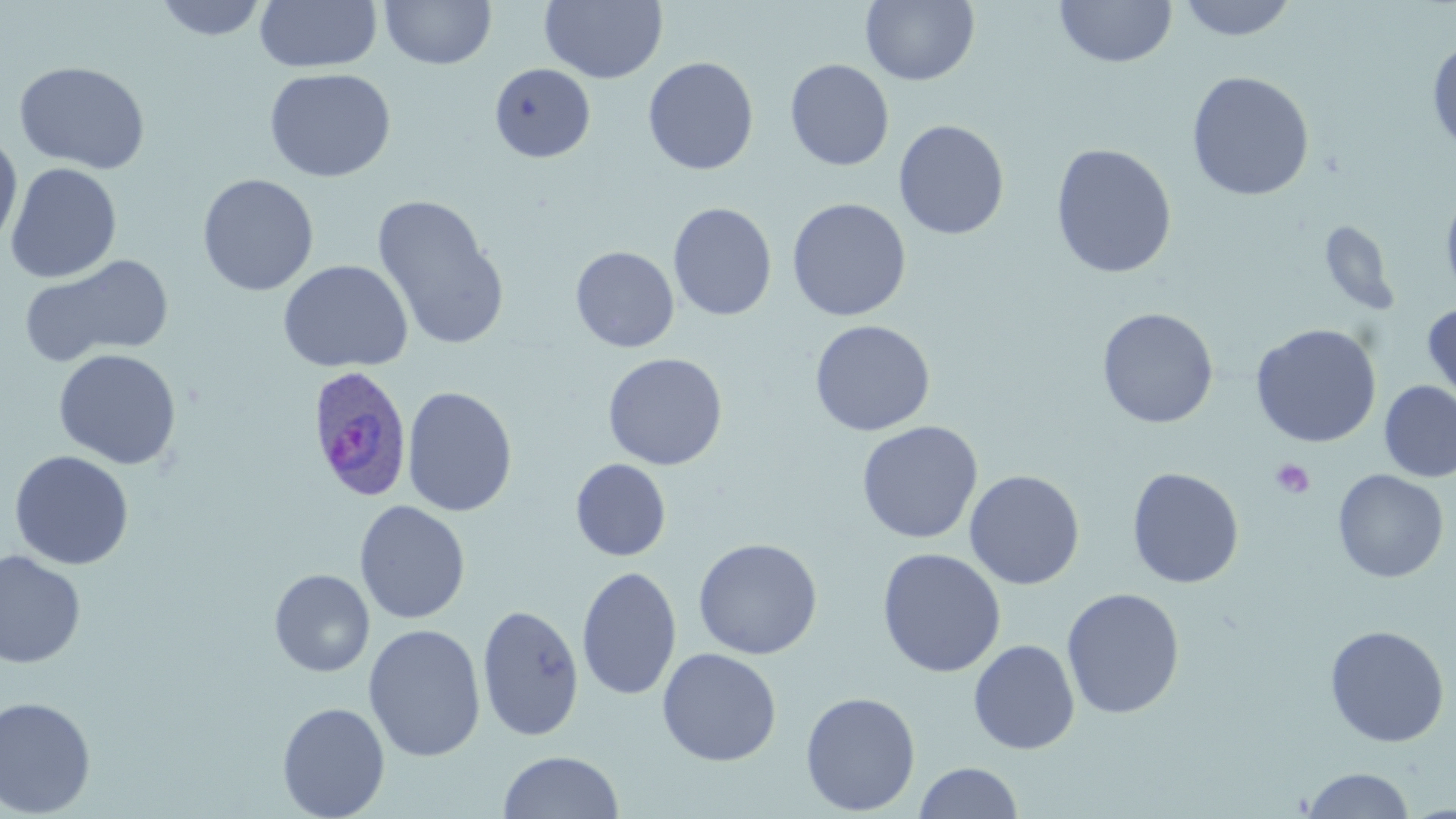

Summary:
  - Coordinate format: approximate bounding boxes as named x1/y1/x2/y2 corners in pixels
  - Uninfected red blood cell locations: (x1=154, y1=0, x2=269, y2=41), (x1=253, y1=0, x2=382, y2=73), (x1=380, y1=0, x2=497, y2=69), (x1=540, y1=0, x2=667, y2=84), (x1=1177, y1=0, x2=1298, y2=41), (x1=861, y1=1, x2=980, y2=86), (x1=1055, y1=1, x2=1177, y2=68), (x1=1427, y1=38, x2=1456, y2=156), (x1=643, y1=56, x2=759, y2=175), (x1=785, y1=59, x2=894, y2=171), (x1=14, y1=60, x2=150, y2=175), (x1=489, y1=63, x2=596, y2=163), (x1=263, y1=67, x2=396, y2=182), (x1=1187, y1=71, x2=1315, y2=201), (x1=893, y1=119, x2=1009, y2=240), (x1=0, y1=132, x2=23, y2=251), (x1=1050, y1=143, x2=1177, y2=279), (x1=5, y1=163, x2=122, y2=283), (x1=197, y1=173, x2=319, y2=297), (x1=1440, y1=186, x2=1456, y2=306), (x1=371, y1=194, x2=508, y2=350), (x1=787, y1=198, x2=911, y2=322), (x1=668, y1=203, x2=778, y2=321), (x1=1318, y1=222, x2=1401, y2=315), (x1=570, y1=246, x2=679, y2=353), (x1=18, y1=254, x2=175, y2=368), (x1=278, y1=259, x2=413, y2=373), (x1=1422, y1=303, x2=1456, y2=410), (x1=1097, y1=308, x2=1219, y2=428), (x1=809, y1=319, x2=935, y2=436), (x1=1250, y1=323, x2=1382, y2=448), (x1=53, y1=348, x2=181, y2=470), (x1=603, y1=352, x2=728, y2=470), (x1=1379, y1=380, x2=1456, y2=483), (x1=402, y1=386, x2=518, y2=517), (x1=857, y1=421, x2=983, y2=544), (x1=9, y1=450, x2=134, y2=570), (x1=570, y1=458, x2=671, y2=562), (x1=1126, y1=467, x2=1245, y2=589), (x1=1333, y1=469, x2=1449, y2=583), (x1=964, y1=470, x2=1085, y2=590), (x1=354, y1=500, x2=471, y2=624), (x1=693, y1=537, x2=823, y2=660), (x1=877, y1=547, x2=1006, y2=677), (x1=0, y1=551, x2=86, y2=669), (x1=576, y1=565, x2=682, y2=701), (x1=269, y1=569, x2=375, y2=677), (x1=1061, y1=587, x2=1186, y2=719), (x1=477, y1=603, x2=585, y2=741), (x1=363, y1=624, x2=486, y2=762), (x1=1324, y1=624, x2=1450, y2=748), (x1=968, y1=639, x2=1080, y2=755), (x1=657, y1=647, x2=782, y2=766), (x1=800, y1=691, x2=921, y2=815), (x1=0, y1=696, x2=97, y2=817), (x1=276, y1=701, x2=390, y2=819), (x1=497, y1=750, x2=624, y2=818), (x1=913, y1=762, x2=1024, y2=818), (x1=1301, y1=767, x2=1415, y2=818)
  - Platelet locations: (x1=1270, y1=458, x2=1315, y2=499)
  - Plasmodium ovale-infected red blood cell locations: (x1=305, y1=365, x2=414, y2=502)
  - Slide-level diagnosis: Plasmodium ovale
  - Stain: May-Grünwald-Giemsa
  - Field of view: one of a larger specimen
  - Modality: optical microscopy
  - Magnification: 1000x
  - Image size: 1456×819 pixels
  - Preparation: thin blood film